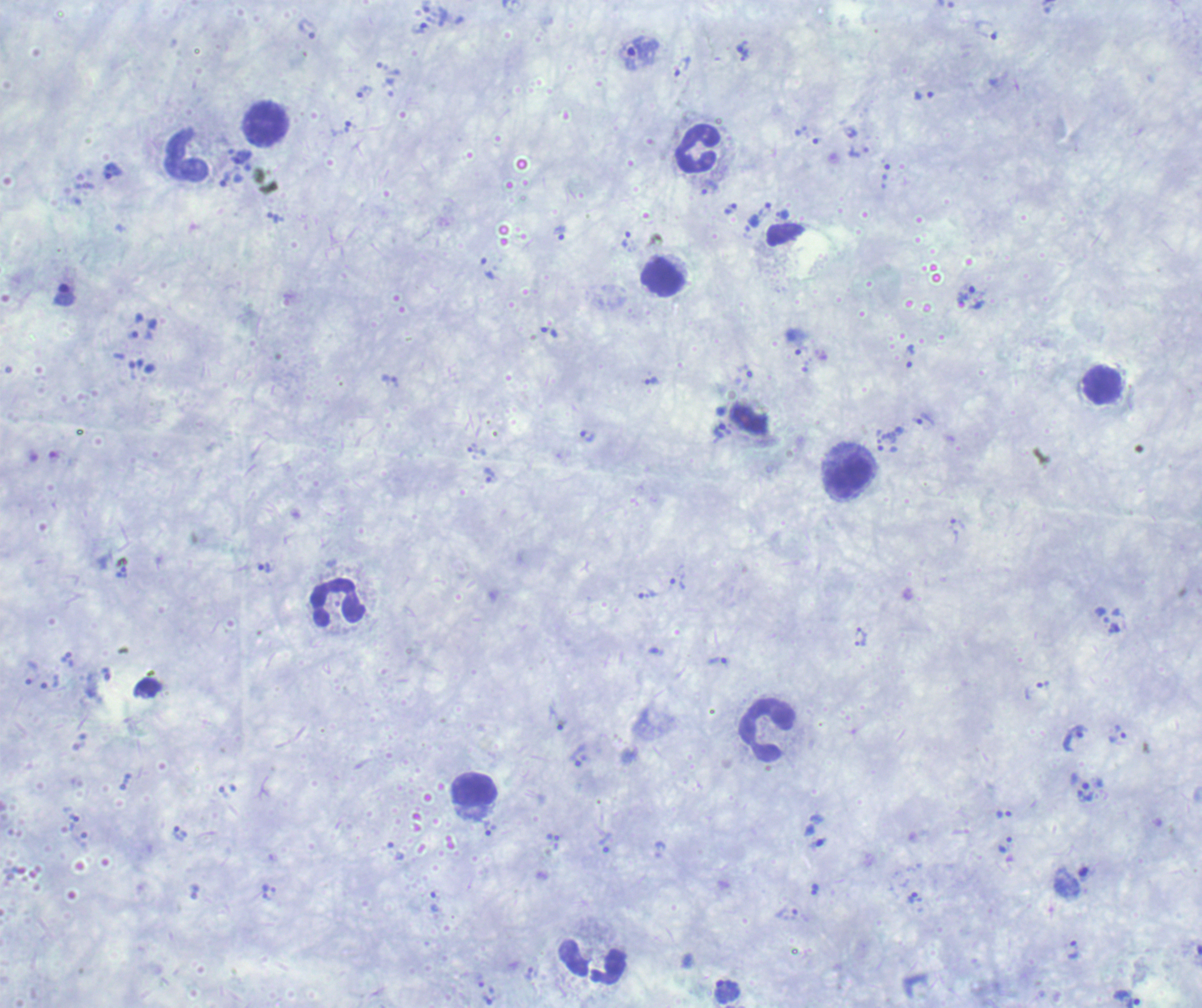

coordinate format = approximate centers as (x, y) in pixels
leukocyte locations = (266, 124), (698, 149), (186, 155), (663, 277), (1102, 385), (850, 477), (337, 603), (765, 730), (475, 790), (592, 961)
trophozoite locations = (419, 29), (308, 30), (743, 50), (638, 54), (683, 67), (364, 95), (341, 128), (112, 172), (226, 180), (731, 207), (559, 234), (626, 239), (488, 268), (966, 291), (550, 332), (909, 356), (651, 381), (925, 420), (721, 432), (586, 436), (477, 451), (488, 476), (264, 567), (123, 573), (679, 584), (648, 596), (719, 662), (1075, 737), (1117, 738), (576, 758), (1004, 814), (487, 827), (180, 833), (605, 843), (1005, 844), (915, 898), (1074, 950), (727, 991), (1126, 997)
magnification = 100x
field of view = one from this slide
context = previously used in a real diagnosis
stain = Romanowsky
result = Plasmodium parasites identified
background quality = poor
image size = 1202×1008 pixels
preparation = thick smear of blood